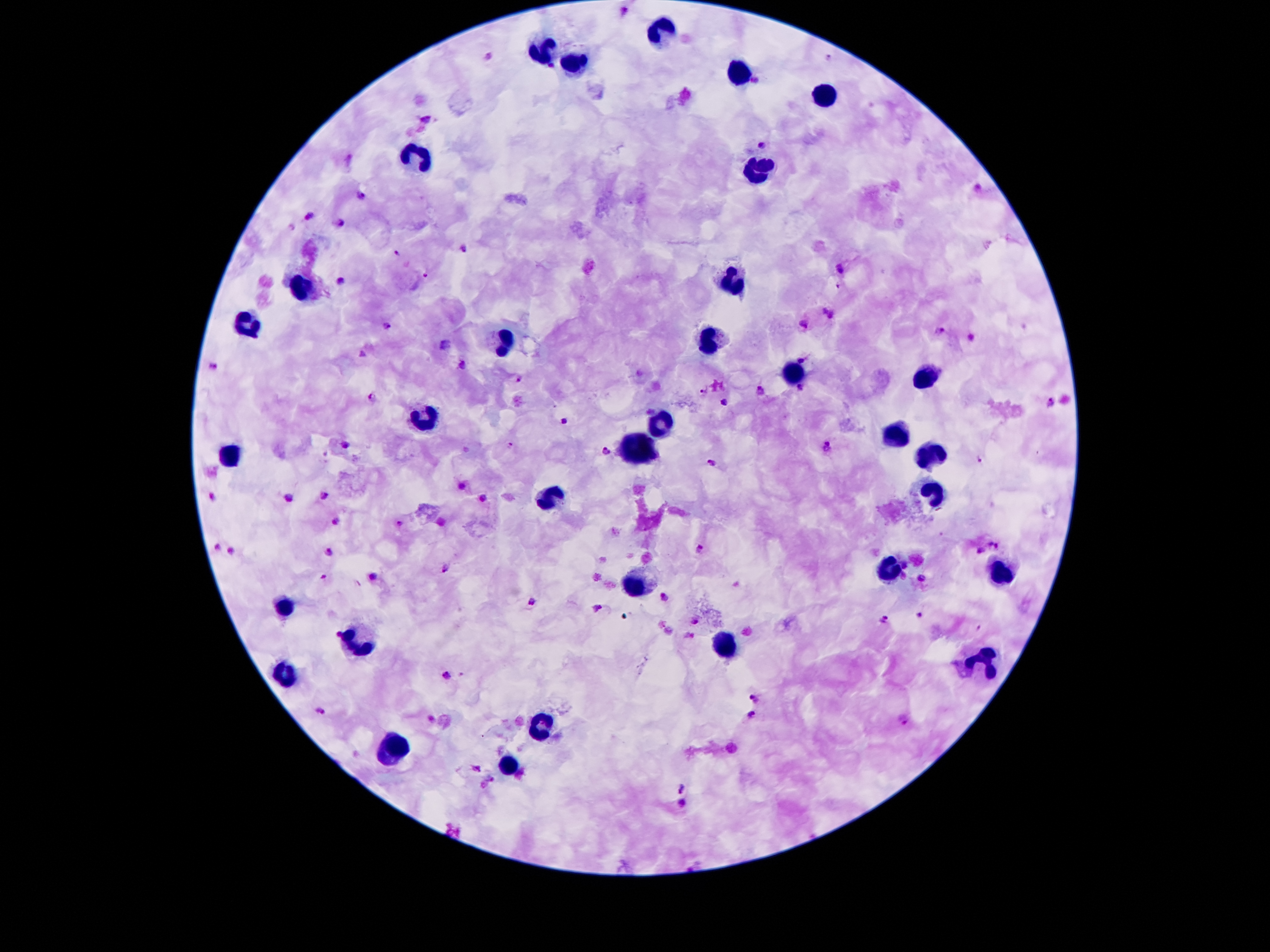
coordinate format = approximate object centers, in pixels from the top-left corner
leukocyte locations = (x=662, y=30), (x=542, y=48), (x=572, y=66), (x=741, y=73), (x=828, y=94), (x=416, y=154), (x=759, y=172), (x=736, y=282), (x=302, y=292), (x=247, y=325), (x=710, y=339), (x=507, y=343), (x=790, y=372), (x=923, y=377), (x=422, y=420), (x=663, y=423), (x=893, y=436), (x=641, y=447), (x=230, y=454), (x=931, y=454), (x=933, y=487), (x=547, y=498), (x=887, y=570), (x=992, y=573), (x=633, y=585), (x=286, y=607), (x=356, y=640), (x=725, y=646), (x=987, y=662), (x=286, y=676), (x=543, y=724), (x=396, y=747), (x=510, y=764)
malaria parasite locations = (x=626, y=11), (x=489, y=54), (x=827, y=57), (x=552, y=65), (x=755, y=80), (x=426, y=117), (x=763, y=144), (x=350, y=159), (x=977, y=189), (x=360, y=195), (x=309, y=215), (x=340, y=222), (x=464, y=248), (x=396, y=254), (x=841, y=269), (x=426, y=277), (x=340, y=281), (x=841, y=284), (x=828, y=312), (x=805, y=324), (x=387, y=325), (x=941, y=331), (x=970, y=338), (x=447, y=345), (x=363, y=354), (x=801, y=359), (x=464, y=364), (x=213, y=365), (x=518, y=379), (x=800, y=388), (x=704, y=390), (x=758, y=390), (x=372, y=395), (x=725, y=402), (x=1051, y=403), (x=564, y=421), (x=345, y=443), (x=509, y=444), (x=827, y=447), (x=607, y=451), (x=981, y=457), (x=712, y=463), (x=462, y=486), (x=324, y=494), (x=212, y=496), (x=289, y=497), (x=483, y=498), (x=335, y=522), (x=399, y=522), (x=994, y=545), (x=217, y=546), (x=701, y=547), (x=329, y=551), (x=980, y=551), (x=230, y=552), (x=905, y=565), (x=444, y=569), (x=903, y=574), (x=323, y=577), (x=372, y=577), (x=922, y=577), (x=665, y=597), (x=532, y=603), (x=595, y=607), (x=918, y=614), (x=884, y=618), (x=694, y=621), (x=979, y=627), (x=447, y=675), (x=756, y=700), (x=321, y=710), (x=752, y=716), (x=430, y=719), (x=901, y=719), (x=476, y=769), (x=492, y=779), (x=484, y=785), (x=682, y=787), (x=683, y=802)
preparation = thick blood smear
stain = Giemsa
capture = smartphone camera through the microscope eyepiece
field of view = one from this slide
patient malaria status = infected with Plasmodium falciparum
image size = 1270×952 pixels
magnification = 100x